Locate every blood parasite and identify its species.
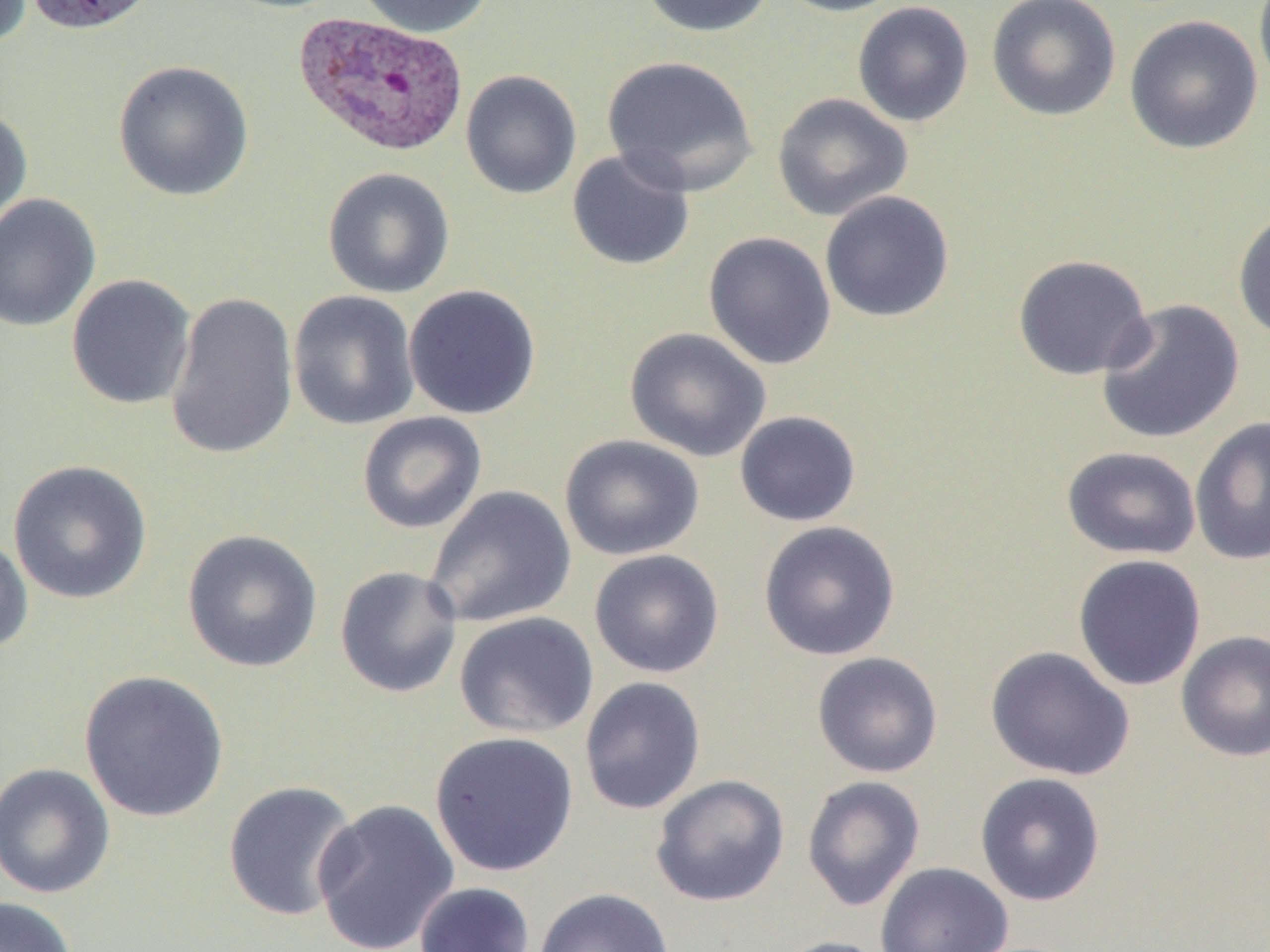
Approximate bounding boxes as (x1, y1, x2, y2) in pixels.
Plasmodium vivax-infected red blood cells: (292, 10, 469, 158).
No Plasmodium falciparum, Plasmodium ovale, Plasmodium malariae, Babesia divergens, or Trypanosoma brucei observed.

slide_level_diagnosis: Plasmodium vivax
uninfected_red_blood_cell_locations: 'approximate bounding boxes as (x1, y1, x2, y2) in pixels: (0, 0, 33, 50), (24, 0, 159, 35), (354, 0, 494, 38), (638, 0, 777, 38), (774, 0, 912, 17), (986, 0, 1121, 122), (1253, 0, 1270, 102), (852, 1, 974, 127), (1124, 14, 1264, 155), (601, 54, 759, 196), (113, 60, 255, 202), (460, 70, 582, 200), (772, 93, 913, 221), (0, 105, 32, 239), (566, 148, 696, 271), (322, 167, 455, 298), (819, 190, 954, 323), (0, 193, 101, 332), (1232, 205, 1270, 342), (703, 232, 836, 370), (1012, 254, 1154, 381), (65, 274, 197, 410), (403, 284, 542, 420), (287, 290, 420, 431), (164, 291, 299, 460), (1095, 298, 1244, 444), (624, 327, 771, 462), (734, 410, 861, 527), (357, 412, 487, 534), (1189, 416, 1270, 566), (559, 434, 704, 560), (1062, 446, 1202, 560), (8, 459, 152, 605), (423, 485, 577, 628), (758, 520, 901, 661), (181, 528, 323, 673), (0, 532, 34, 656), (588, 549, 724, 678), (1072, 553, 1207, 691), (334, 565, 463, 698), (454, 611, 599, 740), (1176, 630, 1270, 762), (985, 646, 1135, 781), (811, 651, 943, 778), (78, 669, 230, 823), (579, 676, 706, 815), (429, 731, 579, 878), (0, 762, 116, 900), (975, 772, 1106, 906), (651, 774, 790, 907), (802, 775, 925, 911), (222, 780, 361, 922), (312, 798, 460, 952), (875, 862, 1013, 952), (413, 882, 536, 952), (534, 887, 675, 952), (0, 895, 79, 952), (771, 936, 895, 952)'
image_size: 1270×952 pixels
modality: light microscopy
magnification: 1000x
field_of_view: single
preparation: thin blood film